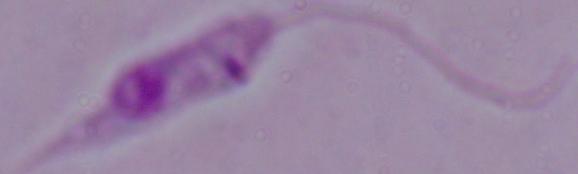
Photomicrograph. A Leishmania parasite is shown. 1000x magnification.